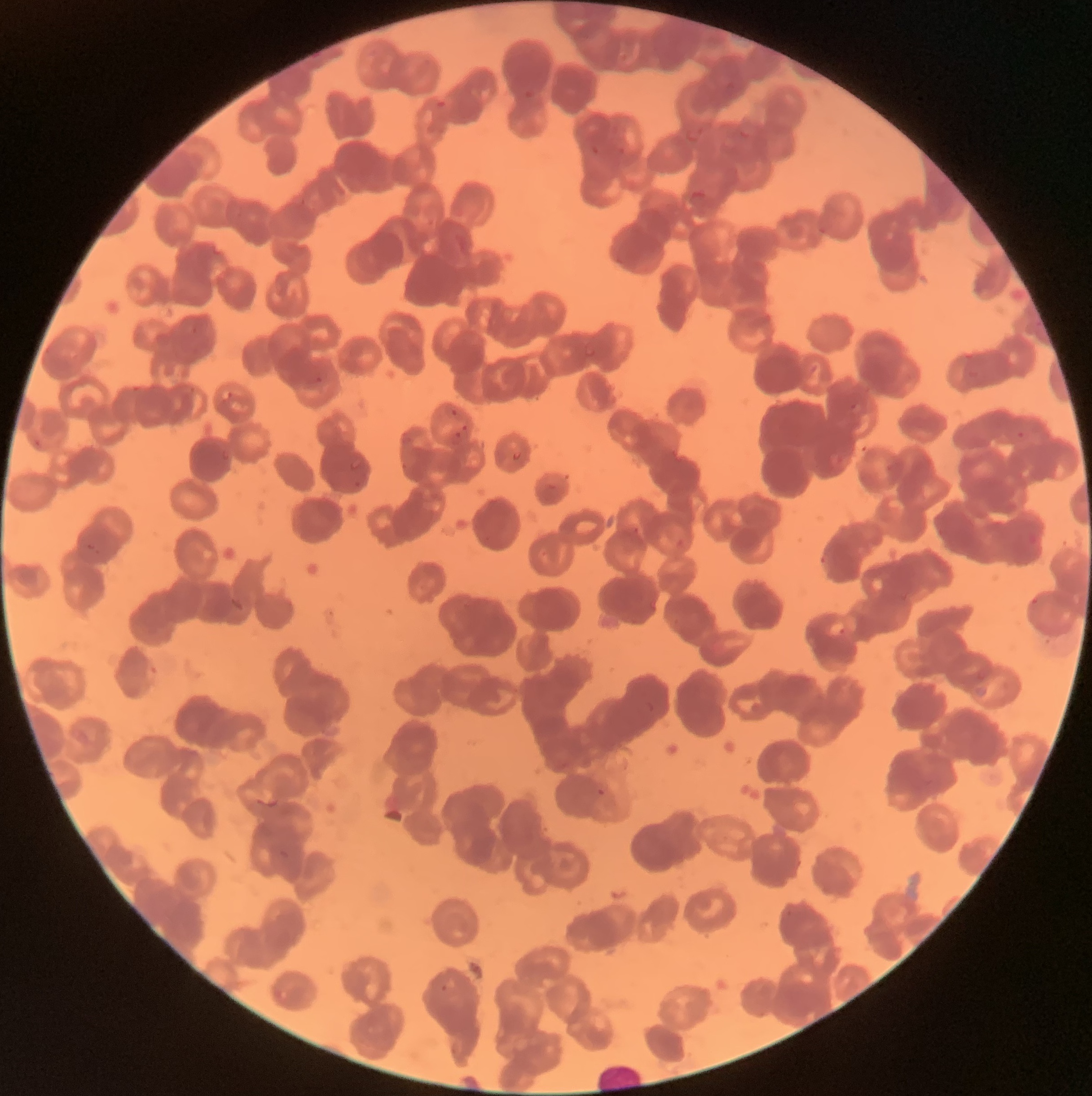 Approximate bounding boxes as (x1, y1, x2, y2) in pixels. Plasmodium parasite locations: (522, 89, 535, 101), (435, 99, 448, 109), (684, 124, 705, 144), (313, 375, 324, 385), (220, 389, 234, 402), (850, 402, 862, 415), (450, 409, 458, 417), (461, 423, 469, 433), (1015, 429, 1027, 440), (450, 431, 463, 446), (350, 459, 363, 471), (87, 542, 96, 551), (820, 551, 830, 567), (827, 620, 846, 639), (142, 657, 160, 687), (596, 787, 606, 797), (440, 977, 456, 995). Image is 1092×1096 pixels. Thin blood film. Light microscopy. The red blood cells show rouleaux formation.